Classify this cell by malaria status.
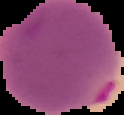
It is parasitized.

Image is 124×115 pixels. Cell region segmented out of the field of view; the surrounding area is masked to black. From a thin blood film.